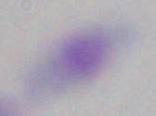
identification = Toxoplasma gondii
modality = micrograph
magnification = 1000x